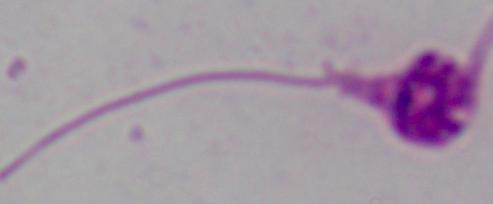

magnification = 1000x
modality = photomicrograph
identification = Leishmania